Classify this cell by malaria status.
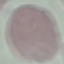

Uninfected.

Summary:
  - Capture: smartphone camera at the microscope eyepiece
  - Image type: automatically extracted cell patch, resized to 64 × 64 pixels
  - Stain: Giemsa
  - Preparation: thin blood smear